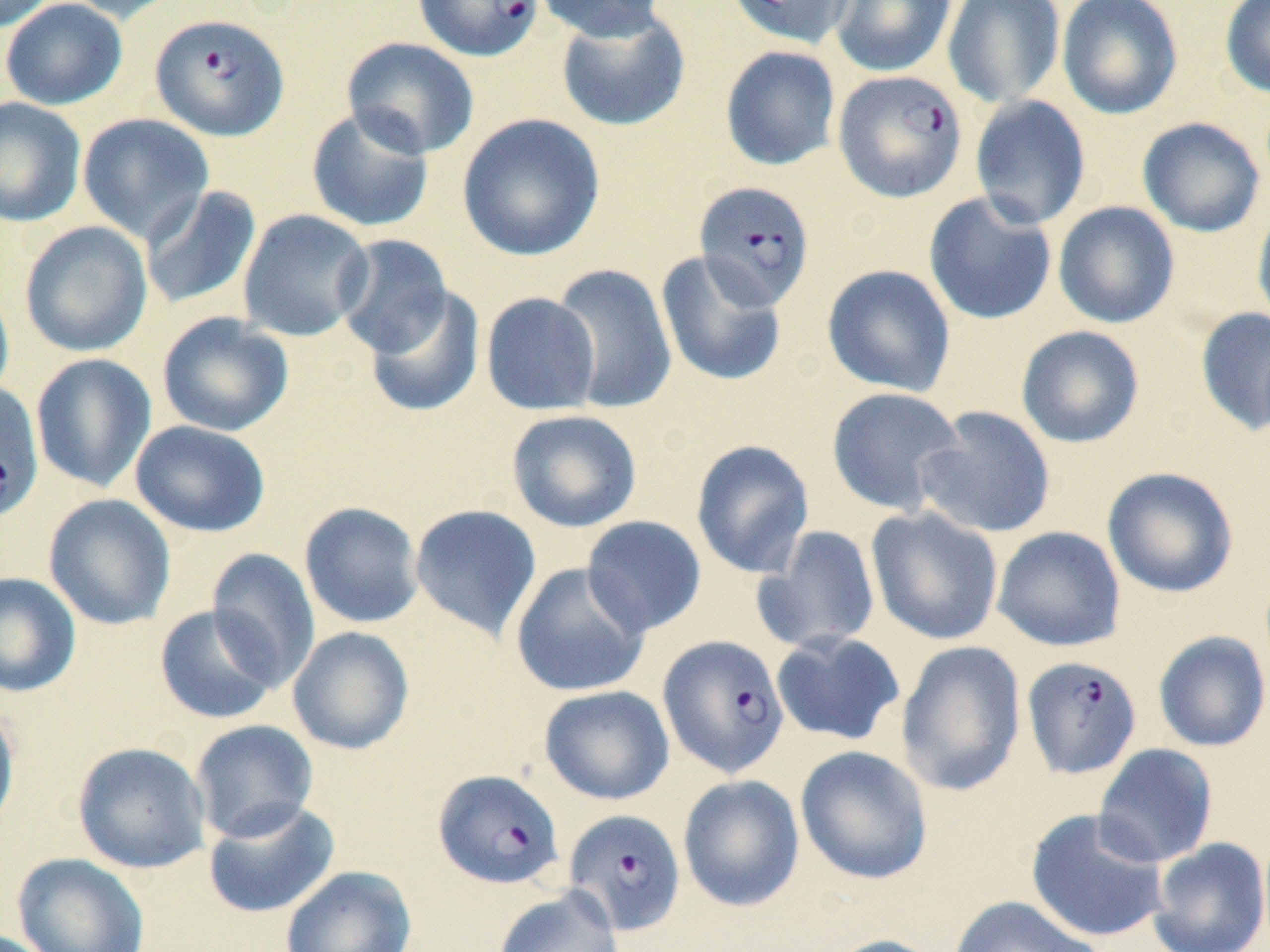

slide-level diagnosis = Plasmodium falciparum
field of view = single
stain = May-Grünwald-Giemsa
image size = 1270×952 pixels
preparation = thin blood smear
modality = optical microscopy
Plasmodium falciparum-infected red blood cell locations = approximate bounding boxes as named x1/y1/x2/y2 corners in pixels: (x1=412, y1=0, x2=542, y2=62), (x1=149, y1=12, x2=290, y2=140), (x1=833, y1=69, x2=968, y2=203), (x1=693, y1=181, x2=816, y2=310), (x1=0, y1=379, x2=43, y2=524), (x1=658, y1=634, x2=790, y2=778), (x1=1021, y1=655, x2=1142, y2=779), (x1=433, y1=768, x2=565, y2=890), (x1=563, y1=809, x2=686, y2=936)
magnification = 1000x
uninfected red blood cell locations = approximate bounding boxes as named x1/y1/x2/y2 corners in pixels: (x1=0, y1=0, x2=58, y2=34), (x1=1, y1=0, x2=127, y2=110), (x1=62, y1=0, x2=187, y2=24), (x1=533, y1=0, x2=669, y2=42), (x1=725, y1=0, x2=858, y2=49), (x1=830, y1=0, x2=957, y2=77), (x1=942, y1=0, x2=1066, y2=109), (x1=1220, y1=0, x2=1270, y2=99), (x1=1056, y1=1, x2=1183, y2=120), (x1=555, y1=8, x2=691, y2=132), (x1=341, y1=37, x2=480, y2=159), (x1=719, y1=45, x2=841, y2=171), (x1=969, y1=95, x2=1091, y2=230), (x1=0, y1=97, x2=86, y2=227), (x1=304, y1=106, x2=436, y2=234), (x1=456, y1=112, x2=605, y2=262), (x1=77, y1=113, x2=214, y2=244), (x1=1137, y1=117, x2=1265, y2=237), (x1=140, y1=185, x2=262, y2=311), (x1=923, y1=191, x2=1058, y2=326), (x1=1251, y1=199, x2=1270, y2=333), (x1=1052, y1=201, x2=1181, y2=329), (x1=239, y1=208, x2=374, y2=342), (x1=19, y1=221, x2=152, y2=357), (x1=333, y1=234, x2=453, y2=358), (x1=656, y1=250, x2=788, y2=387), (x1=550, y1=263, x2=678, y2=415), (x1=822, y1=264, x2=956, y2=397), (x1=0, y1=279, x2=14, y2=407), (x1=362, y1=285, x2=486, y2=418), (x1=481, y1=292, x2=601, y2=416), (x1=1195, y1=306, x2=1270, y2=436), (x1=157, y1=311, x2=294, y2=438), (x1=1016, y1=325, x2=1144, y2=448), (x1=30, y1=353, x2=157, y2=493), (x1=825, y1=387, x2=966, y2=516), (x1=915, y1=405, x2=1056, y2=539), (x1=506, y1=409, x2=642, y2=533), (x1=130, y1=420, x2=271, y2=538), (x1=690, y1=439, x2=815, y2=579), (x1=1102, y1=466, x2=1239, y2=598), (x1=43, y1=493, x2=176, y2=631), (x1=299, y1=501, x2=425, y2=629), (x1=409, y1=504, x2=542, y2=642), (x1=866, y1=507, x2=1004, y2=645), (x1=581, y1=516, x2=707, y2=637), (x1=754, y1=525, x2=880, y2=653), (x1=992, y1=526, x2=1126, y2=652), (x1=206, y1=548, x2=321, y2=689), (x1=510, y1=563, x2=650, y2=698), (x1=0, y1=571, x2=82, y2=698), (x1=153, y1=605, x2=282, y2=726), (x1=288, y1=626, x2=415, y2=755), (x1=770, y1=630, x2=906, y2=746), (x1=1153, y1=630, x2=1270, y2=753), (x1=895, y1=640, x2=1027, y2=797), (x1=538, y1=685, x2=675, y2=805), (x1=0, y1=704, x2=21, y2=838), (x1=190, y1=720, x2=319, y2=843), (x1=72, y1=741, x2=211, y2=874), (x1=1093, y1=743, x2=1219, y2=868), (x1=795, y1=745, x2=933, y2=886), (x1=678, y1=774, x2=805, y2=912), (x1=203, y1=800, x2=340, y2=918), (x1=1025, y1=808, x2=1170, y2=943), (x1=1147, y1=837, x2=1270, y2=952), (x1=12, y1=852, x2=149, y2=952), (x1=280, y1=865, x2=417, y2=952), (x1=493, y1=886, x2=623, y2=952), (x1=948, y1=895, x2=1104, y2=952), (x1=824, y1=934, x2=945, y2=952)